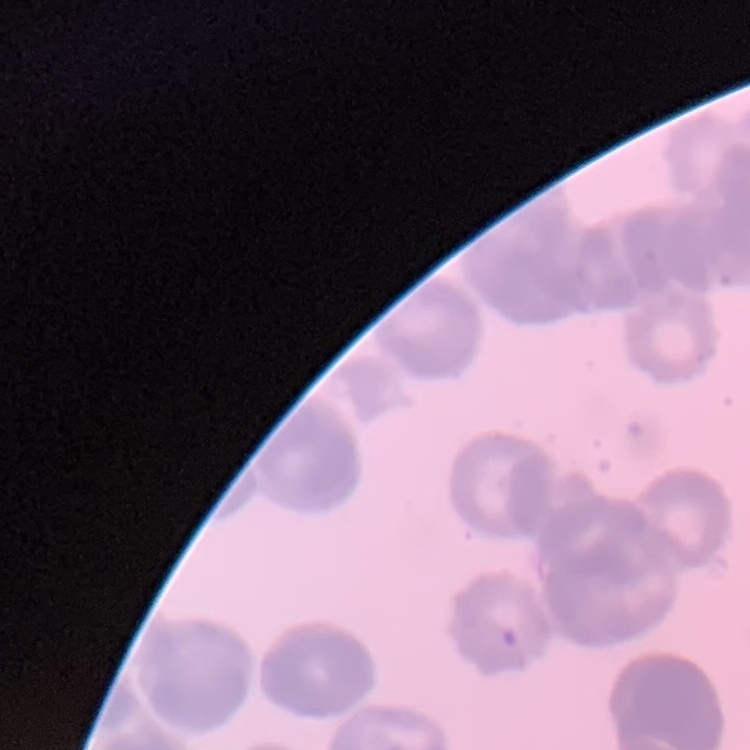
The red blood cells exhibit rouleaux formation. One tile cut from a larger photomicrograph. Thin blood smear. Stained with either Field's or Giemsa.